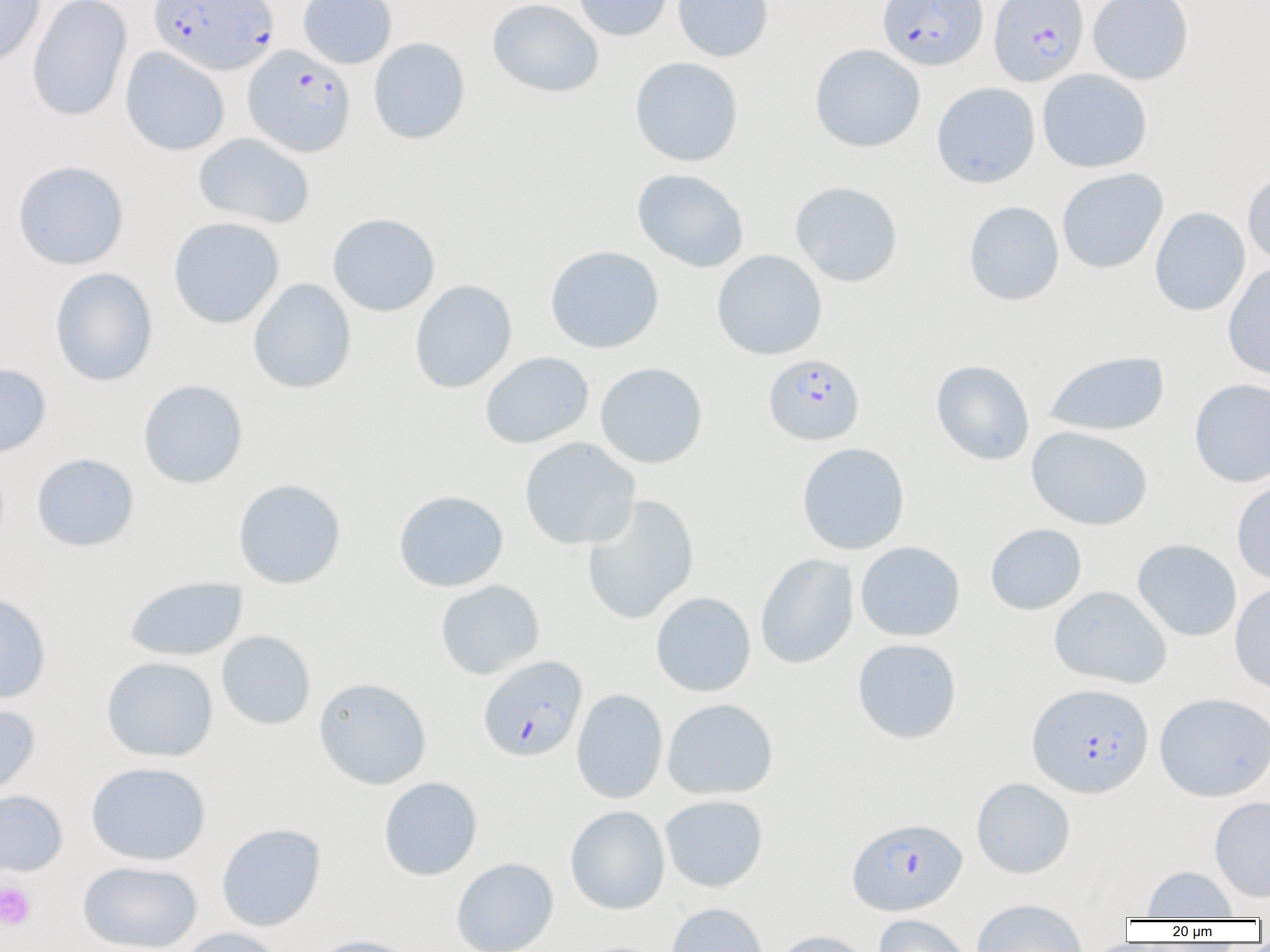

Approximate bounding boxes as named x1/y1/x2/y2 corners in pixels. Platelet locations: (x1=0, y1=881, x2=35, y2=930). Uninfected red blood cell locations: (x1=0, y1=0, x2=45, y2=68), (x1=26, y1=0, x2=132, y2=122), (x1=298, y1=0, x2=397, y2=68), (x1=487, y1=0, x2=604, y2=97), (x1=573, y1=0, x2=673, y2=41), (x1=673, y1=0, x2=773, y2=62), (x1=1088, y1=0, x2=1193, y2=84), (x1=369, y1=37, x2=470, y2=144), (x1=810, y1=43, x2=926, y2=152), (x1=120, y1=47, x2=229, y2=156), (x1=630, y1=56, x2=743, y2=166), (x1=1037, y1=69, x2=1153, y2=173), (x1=932, y1=82, x2=1040, y2=188), (x1=193, y1=133, x2=314, y2=229), (x1=11, y1=160, x2=130, y2=269), (x1=1057, y1=168, x2=1169, y2=274), (x1=632, y1=169, x2=749, y2=273), (x1=1243, y1=170, x2=1270, y2=270), (x1=789, y1=181, x2=903, y2=287), (x1=964, y1=201, x2=1064, y2=305), (x1=1150, y1=207, x2=1250, y2=316), (x1=327, y1=213, x2=440, y2=316), (x1=168, y1=216, x2=284, y2=329), (x1=545, y1=245, x2=664, y2=354), (x1=712, y1=249, x2=827, y2=360), (x1=1223, y1=263, x2=1270, y2=380), (x1=50, y1=267, x2=158, y2=386), (x1=248, y1=278, x2=356, y2=393), (x1=409, y1=280, x2=517, y2=393), (x1=1044, y1=350, x2=1170, y2=436), (x1=480, y1=351, x2=594, y2=449), (x1=931, y1=360, x2=1034, y2=465), (x1=0, y1=362, x2=51, y2=457), (x1=594, y1=362, x2=708, y2=468), (x1=1189, y1=378, x2=1270, y2=487), (x1=138, y1=379, x2=248, y2=488), (x1=1026, y1=426, x2=1153, y2=530), (x1=519, y1=437, x2=640, y2=550), (x1=797, y1=442, x2=910, y2=555), (x1=31, y1=453, x2=139, y2=552), (x1=233, y1=478, x2=346, y2=589), (x1=1231, y1=479, x2=1270, y2=585), (x1=394, y1=490, x2=508, y2=592), (x1=581, y1=494, x2=699, y2=625), (x1=985, y1=523, x2=1086, y2=615), (x1=1132, y1=539, x2=1242, y2=641), (x1=855, y1=541, x2=965, y2=641), (x1=755, y1=553, x2=858, y2=669), (x1=124, y1=576, x2=248, y2=661), (x1=436, y1=579, x2=544, y2=679), (x1=1230, y1=582, x2=1270, y2=696), (x1=1049, y1=585, x2=1171, y2=688), (x1=0, y1=590, x2=51, y2=703), (x1=651, y1=592, x2=756, y2=696), (x1=216, y1=630, x2=316, y2=730), (x1=852, y1=638, x2=962, y2=744), (x1=101, y1=656, x2=218, y2=762), (x1=314, y1=678, x2=431, y2=789), (x1=571, y1=689, x2=668, y2=804), (x1=1154, y1=692, x2=1270, y2=801), (x1=662, y1=698, x2=778, y2=800), (x1=0, y1=702, x2=41, y2=802), (x1=85, y1=761, x2=211, y2=865), (x1=378, y1=777, x2=482, y2=880), (x1=971, y1=777, x2=1075, y2=878), (x1=0, y1=789, x2=68, y2=878), (x1=659, y1=794, x2=768, y2=892), (x1=1209, y1=795, x2=1270, y2=903), (x1=566, y1=806, x2=669, y2=915), (x1=216, y1=823, x2=326, y2=931), (x1=451, y1=857, x2=559, y2=952), (x1=77, y1=861, x2=202, y2=952), (x1=1141, y1=865, x2=1239, y2=919), (x1=970, y1=900, x2=1088, y2=952), (x1=665, y1=902, x2=769, y2=952), (x1=873, y1=914, x2=975, y2=952), (x1=178, y1=927, x2=286, y2=952), (x1=771, y1=930, x2=875, y2=952), (x1=306, y1=934, x2=423, y2=952). Plasmodium falciparum-infected red blood cell locations: (x1=148, y1=0, x2=278, y2=75), (x1=878, y1=0, x2=987, y2=70), (x1=989, y1=0, x2=1088, y2=86), (x1=243, y1=45, x2=355, y2=157), (x1=763, y1=354, x2=864, y2=445), (x1=478, y1=655, x2=587, y2=761), (x1=1027, y1=682, x2=1154, y2=798), (x1=847, y1=817, x2=967, y2=915). Slide-level diagnosis: Plasmodium falciparum. Image is 1270×952 pixels. One field of a larger specimen. 1000x magnification. Thin blood smear. Light microscopy.